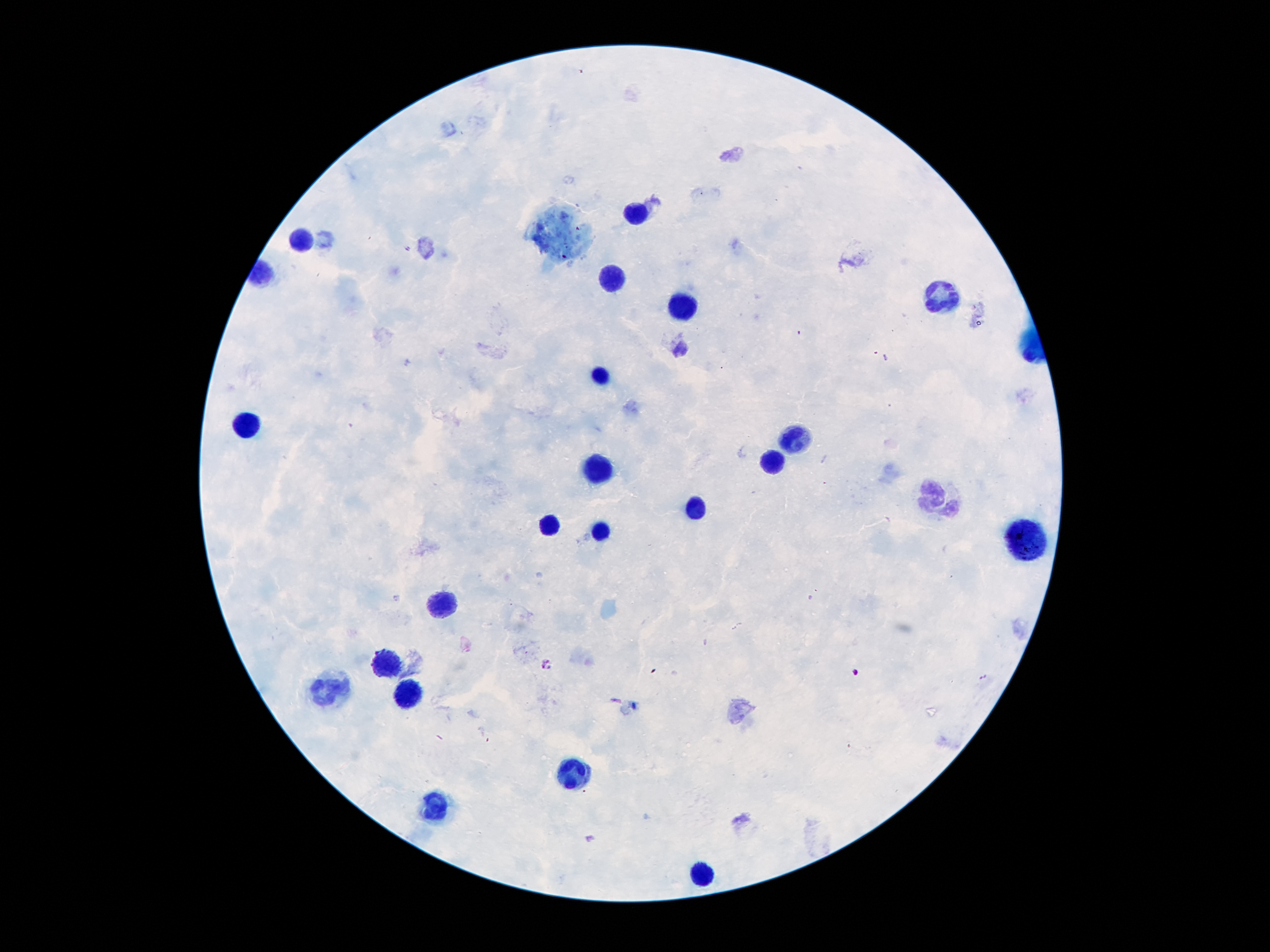
Single field of view. Giemsa stain. 100x magnification. Patient malaria status: positive for Plasmodium falciparum. Smartphone photograph taken through the microscope eyepiece. Image is 1270×952 pixels. Thick blood smear.